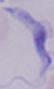
Summary:
  - Magnification: 1000x
  - Identification: trypanosome
  - Modality: micrograph